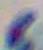
Micrograph. 1000x magnification. Toxoplasma gondii is shown.